Classify this cell by malaria status.
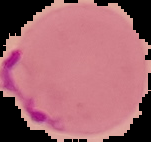
Parasitized.

From a thin blood smear. Image is 151×142 pixels. Cell region segmented out of the field of view; the surrounding area is masked to black.